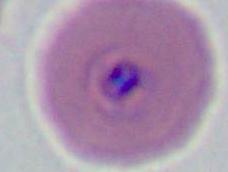

magnification: 400x or 1000x
modality: photomicrograph
identification: Plasmodium